Assess this cell for malaria.
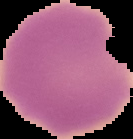
It is uninfected.

{
  "preparation": "thin blood film",
  "image_size": "133×139 pixels",
  "image_type": "segmented cell region with the area outside set to black"
}